Assess this cell for malaria.
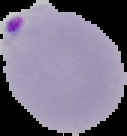

It is parasitized.

From a thin blood smear. Cell region segmented out of the field of view; the surrounding area is masked to black. Image is 127×136 pixels.